Assess this cell for malaria.
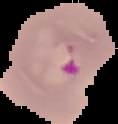

It is parasitized.

Summary:
  - Preparation: thin blood film
  - Image size: 118×124 pixels
  - Image type: segmented cell region on a black background